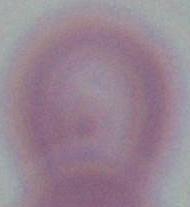
Summary:
  - Magnification: 1000x
  - Modality: photomicrograph
  - Identification: erythrocyte